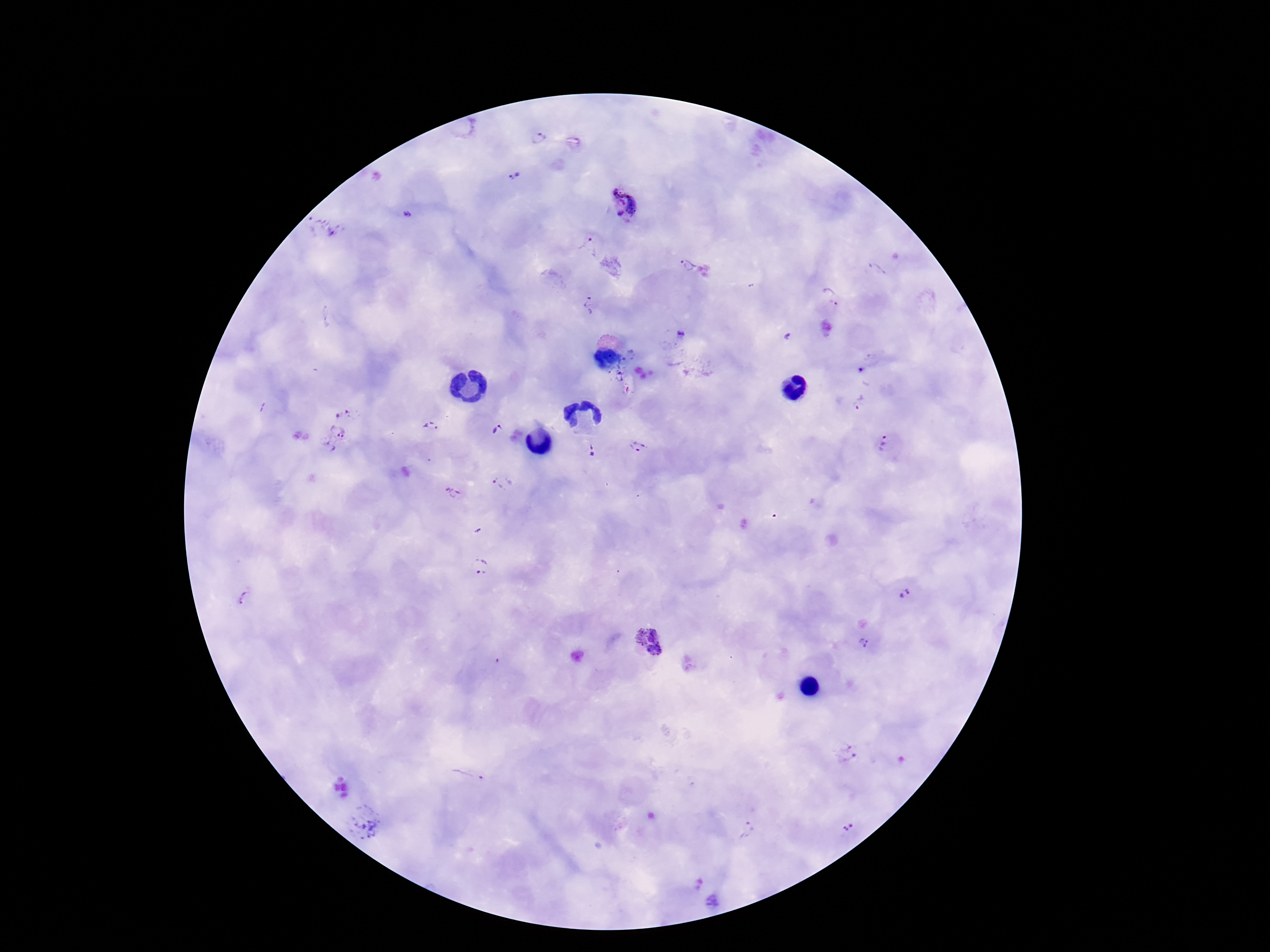

magnification = 100x
patient malaria status = infected
image size = 1270×952 pixels
capture = smartphone camera through the microscope eyepiece
stain = Giemsa
preparation = thick blood film
Plasmodium parasite locations = approximate centers as {x, y} in pixels: {539, 138}, {514, 176}, {623, 201}, {407, 214}, {323, 227}, {589, 245}, {686, 265}, {878, 269}, {830, 297}, {589, 305}, {681, 336}, {622, 380}, {860, 405}, {344, 410}, {432, 427}, {497, 431}, {335, 437}, {886, 443}, {638, 448}, {591, 450}, {502, 482}, {454, 492}, {479, 565}, {904, 595}, {247, 599}, {649, 642}, {864, 642}, {847, 753}, {472, 775}, {362, 822}, {848, 828}, {748, 829}
field of view = one from this slide